Give the position of every leukocyte.
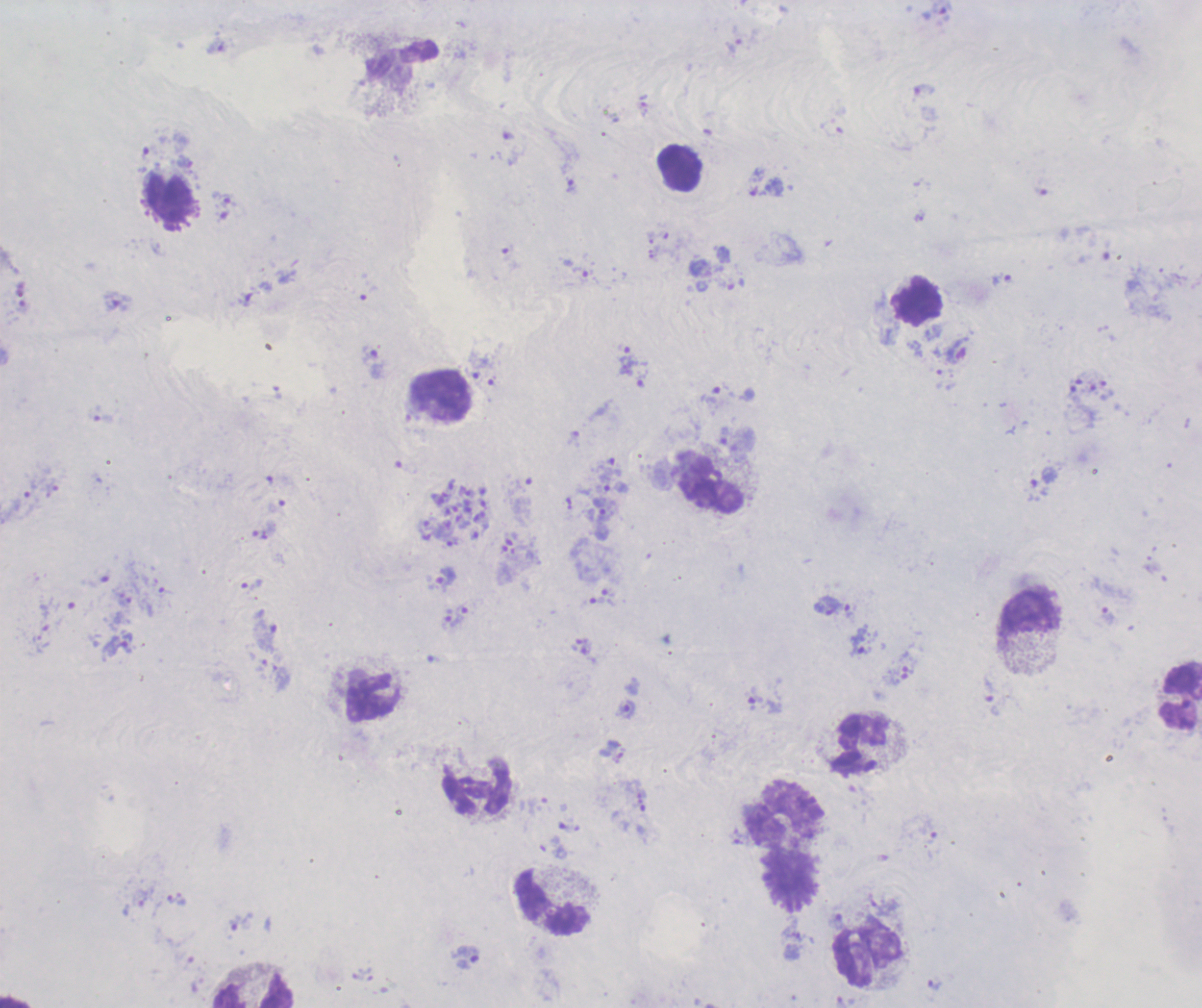
Approximate object centers, in pixels from the top-left corner.
Leukocytes: (x=679, y=168), (x=170, y=200), (x=919, y=300), (x=441, y=395), (x=712, y=485), (x=1031, y=613), (x=1180, y=695), (x=372, y=698), (x=861, y=744), (x=478, y=787), (x=785, y=814), (x=790, y=877), (x=553, y=902), (x=868, y=955), (x=253, y=992).

Approximate object centers, in pixels from the top-left corner. Gametocyte locations: (x=957, y=350). Schizont locations: (x=454, y=513). Trophozoite locations: (x=734, y=46), (x=571, y=186), (x=224, y=200), (x=583, y=275), (x=1002, y=280), (x=118, y=301), (x=627, y=361), (x=372, y=364), (x=100, y=415), (x=1044, y=476), (x=616, y=487), (x=52, y=488), (x=604, y=509), (x=446, y=578), (x=251, y=584), (x=609, y=593), (x=601, y=602), (x=828, y=606), (x=463, y=608), (x=851, y=611), (x=1108, y=615), (x=454, y=618), (x=266, y=637), (x=861, y=641), (x=120, y=644), (x=991, y=697), (x=764, y=702), (x=626, y=710), (x=241, y=922), (x=468, y=957), (x=935, y=983). Life-cycle stages observed: trophozoite, schizont, gametocyte. Thick smear of blood. Romanowsky-stained preparation. Image is 1202×1008 pixels. Result: malaria parasites detected. Previously used in a real diagnosis. One field from this slide. Background quality: unsatisfactory. Captured at 100x magnification.